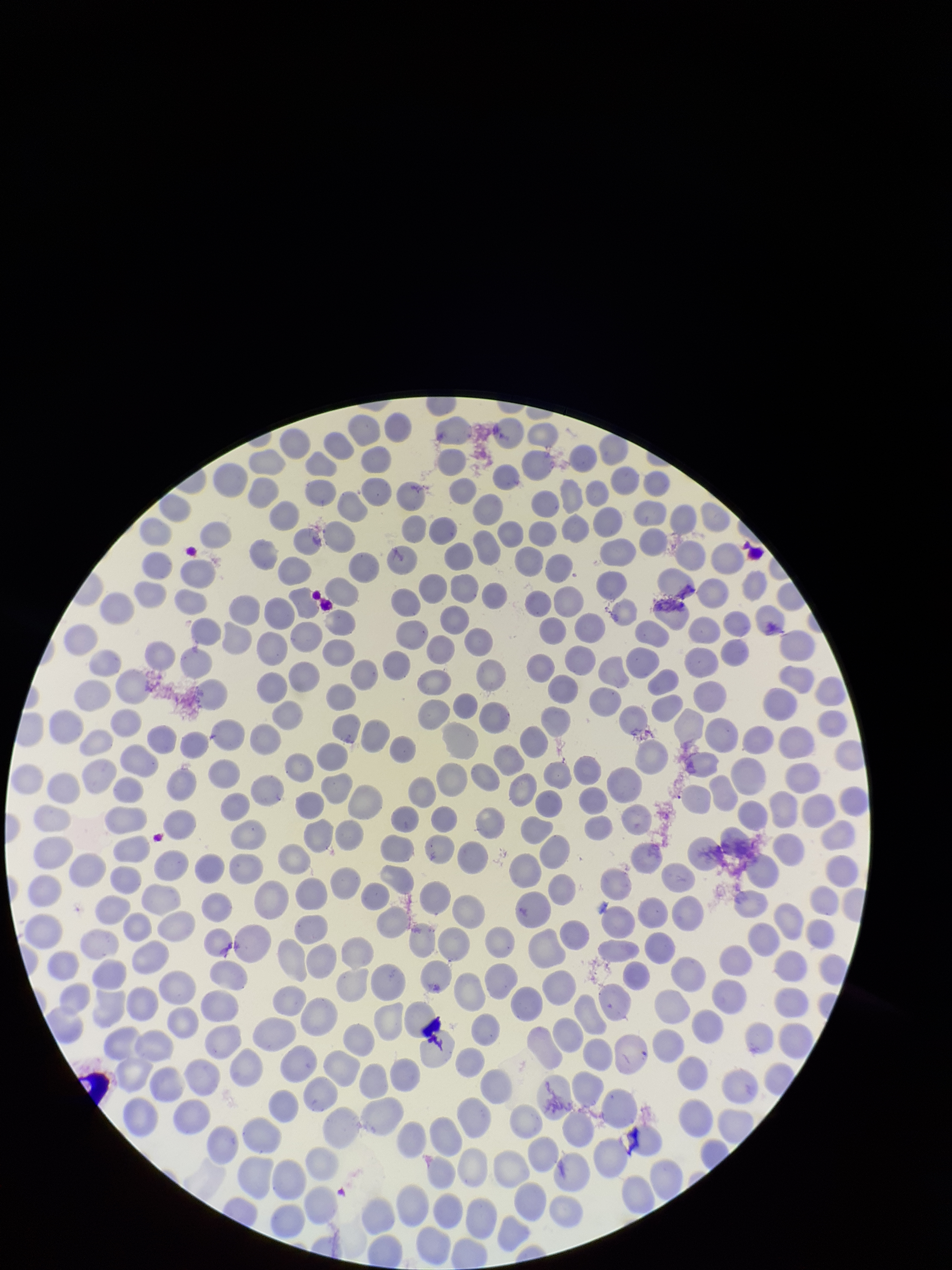

{
  "stain": "Giemsa",
  "parasitized_red_blood_cells": "none detected",
  "capture": "smartphone photograph through the microscope eyepiece",
  "red_blood_cell_count": 351,
  "field_of_view": "one from this slide",
  "parasitized_red_blood_cell_count": 0,
  "patient_malaria_status": "negative",
  "image_size": "952×1270 pixels",
  "preparation": "thin smear"
}